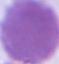

An erythrocyte is shown. Captured at 1000x magnification. Micrograph.